Report the malaria status of this cell.
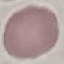
Uninfected.

Giemsa-stained preparation. Automatically extracted cell patch, resized to 64 × 64 pixels. Thin smear of blood. Acquired by smartphone through the microscope eyepiece.